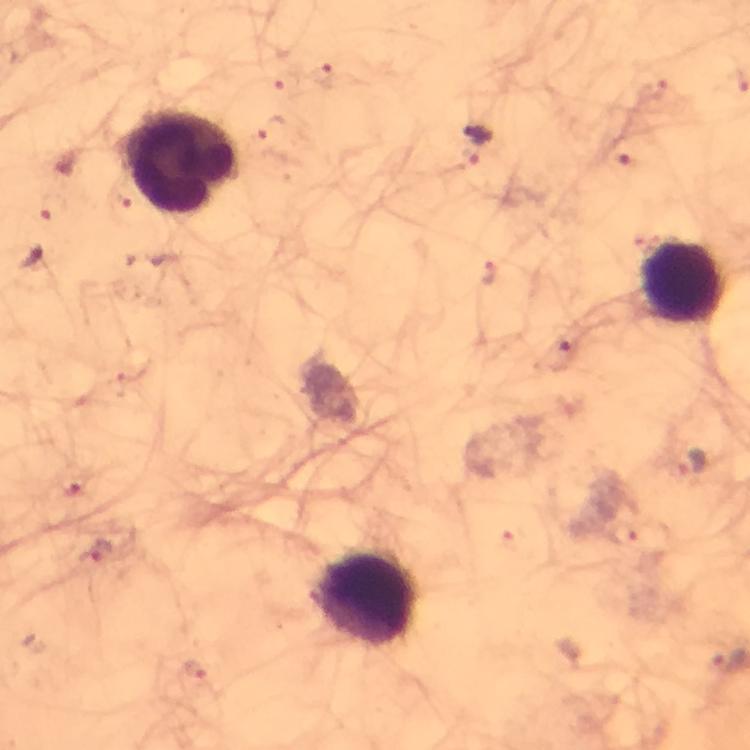

Approximate centers as (x, y) in pixels.
Summary:
  - Leukocyte locations: (180, 162), (682, 283), (365, 597)
  - Malaria parasite locations: (477, 145), (33, 256), (692, 463), (96, 555)
  - Cropped from: a single field of view
  - Immersion oil: applied
  - Stain: Giemsa
  - Image size: 750×750 pixels
  - Capture: smartphone camera through the microscope
  - Preparation: thick smear
  - Magnification: 100x
  - Context: from a diagnostic examination for malaria